Identify the parasite.
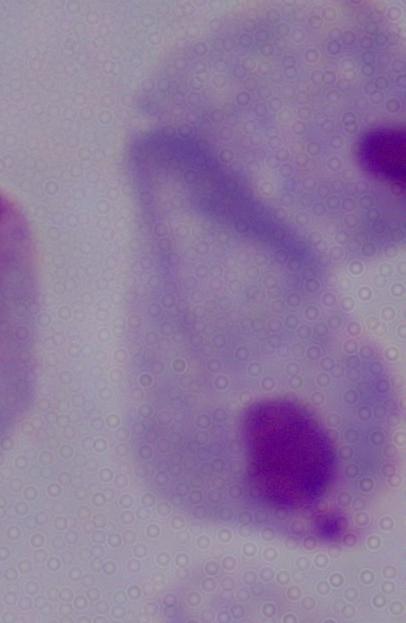
A trichomonad.

Micrograph. Captured at 1000x magnification.